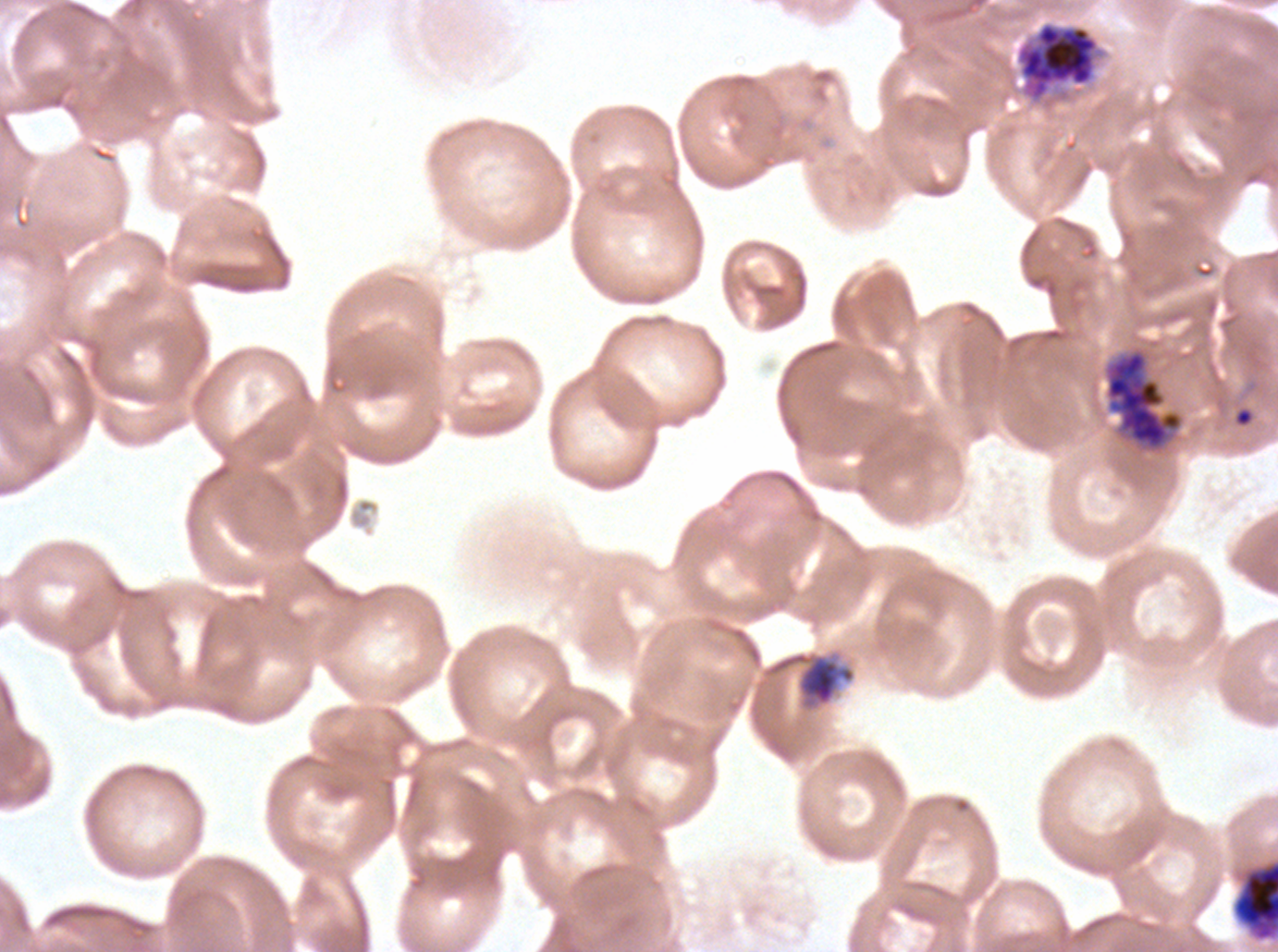

Approximate bounding rectangles given as corner coordinates in pixels from the top-left.
Summary:
  - Late-ring/early-trophozoite locations: (x1=775, y1=652, x2=855, y2=707)
  - Early schizont locations: (x1=1235, y1=862, x2=1277, y2=939)
  - Late schizont locations: (x1=1014, y1=19, x2=1110, y2=111), (x1=1105, y1=350, x2=1182, y2=449)
  - Ring locations: (x1=1232, y1=405, x2=1256, y2=429)
  - Life-cycle stages observed: ring, late-ring/early-trophozoite, early schizont, late schizont
  - Field of view: sub-image separated from a larger composite
  - Preparation: thin blood film
  - Specimen: Plasmodium falciparum from a patient in The Gambia, cultured ex vivo for 24 to 48 hours
  - Stain: Giemsa
  - Image size: 1278×952 pixels